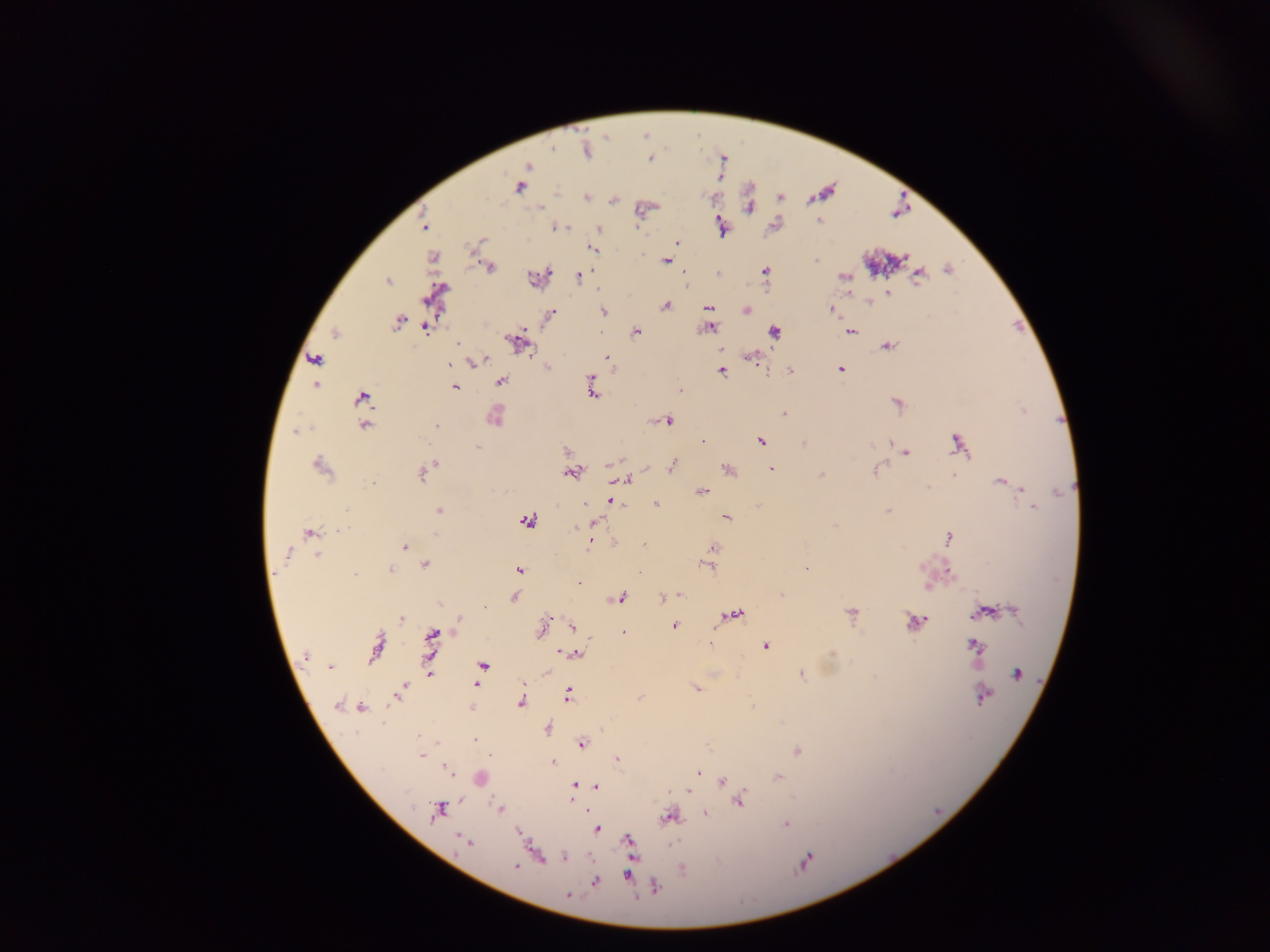

capture = mobile-phone photograph through a microscope
Plasmodium parasite locations = approximate centers as {x, y} in pixels: {649, 159}, {528, 166}, {520, 187}, {586, 197}, {614, 201}, {540, 207}, {750, 207}, {819, 221}, {424, 225}, {721, 226}, {557, 227}, {599, 229}, {678, 243}, {591, 248}, {433, 257}, {815, 260}, {666, 261}, {490, 269}, {948, 269}, {765, 270}, {549, 273}, {919, 275}, {844, 276}, {579, 277}, {388, 281}, {887, 293}, {868, 303}, {665, 306}, {709, 308}, {604, 310}, {746, 310}, {832, 310}, {552, 313}, {398, 322}, {709, 328}, {424, 329}, {636, 331}, {851, 331}, {775, 332}, {335, 333}, {517, 342}, {458, 343}, {886, 347}, {606, 357}, {753, 358}, {316, 359}, {486, 360}, {476, 362}, {547, 367}, {841, 368}, {721, 370}, {790, 371}, {591, 376}, {501, 381}, {316, 385}, {455, 387}, {592, 390}, {680, 390}, {361, 398}, {784, 414}, {495, 417}, {668, 420}, {364, 426}, {436, 426}, {296, 430}, {420, 438}, {702, 441}, {760, 441}, {890, 442}, {804, 443}, {958, 444}, {478, 447}, {566, 451}, {906, 453}, {622, 459}, {435, 464}, {611, 464}, {672, 465}, {321, 467}, {647, 467}, {728, 469}, {772, 469}, {423, 472}, {570, 473}, {821, 476}, {955, 476}, {627, 481}, {371, 482}, {1000, 482}, {928, 487}, {1021, 488}, {703, 491}, {612, 502}, {585, 505}, {656, 505}, {1033, 507}, {439, 510}, {889, 511}, {727, 517}, {526, 521}, {596, 522}, {580, 526}, {576, 528}, {339, 530}, {310, 532}, {436, 534}, {949, 537}, {590, 542}, {404, 547}, {713, 547}, {288, 553}, {317, 556}, {425, 564}, {707, 566}, {806, 569}, {390, 570}, {520, 570}, {949, 571}, {638, 572}, {355, 574}, {579, 584}, {927, 587}, {679, 595}, {781, 595}, {514, 597}, {621, 598}, {662, 598}, {484, 607}, {1014, 611}, {851, 612}, {985, 612}, {736, 614}, {977, 614}, {401, 618}, {925, 618}, {458, 621}, {914, 621}, {573, 626}, {675, 626}, {542, 628}, {624, 632}, {433, 634}, {710, 645}, {976, 645}, {765, 646}, {377, 647}, {564, 653}, {577, 655}, {305, 656}, {330, 666}, {482, 666}, {430, 674}, {1016, 674}, {802, 675}, {476, 684}, {404, 686}, {696, 689}, {568, 694}, {398, 695}, {982, 696}, {638, 698}, {521, 701}, {337, 705}, {362, 707}, {471, 708}, {547, 728}, {418, 735}, {475, 740}, {582, 744}, {797, 751}, {491, 755}, {421, 756}, {617, 760}, {552, 763}, {448, 770}, {698, 772}, {778, 776}, {480, 779}, {722, 782}, {574, 786}, {596, 786}, {688, 791}, {572, 799}, {739, 800}, {500, 809}, {437, 811}, {705, 814}, {669, 817}, {785, 824}, {597, 829}, {518, 833}, {629, 840}, {465, 841}, {565, 857}, {806, 860}, {516, 866}, {629, 875}, {596, 882}, {656, 887}, {568, 895}
field of view = single
image size = 1270×952 pixels
country = Ghana
preparation = thick blood smear